Outline each blood parasite and name the species.
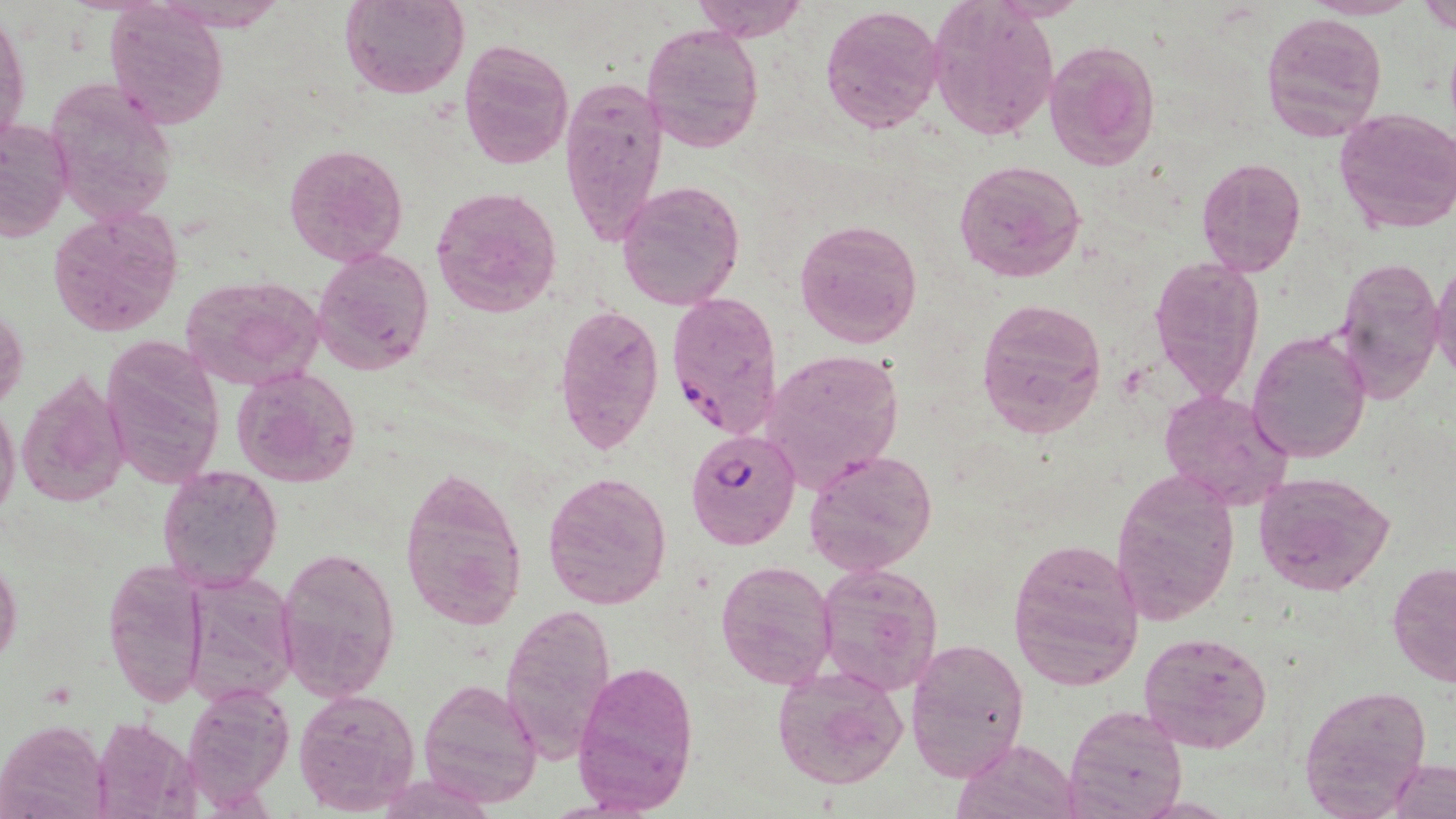

Approximate bounding boxes as [x1, y1, x2, y2] in pixels.
Plasmodium falciparum-infected red blood cells: [664, 289, 782, 441], [685, 429, 800, 548].
No Plasmodium ovale, Plasmodium malariae, Plasmodium vivax, Babesia divergens, or Trypanosoma brucei observed.

Uninfected red blood cell locations: [340, 0, 470, 100], [693, 0, 809, 43], [1419, 0, 1456, 34], [926, 1, 1058, 141], [103, 2, 229, 126], [1, 5, 29, 150], [820, 6, 946, 132], [1259, 10, 1387, 143], [642, 22, 762, 150], [458, 38, 574, 170], [1044, 39, 1162, 171], [43, 74, 179, 225], [559, 74, 668, 252], [1334, 106, 1456, 235], [0, 119, 73, 242], [284, 141, 409, 269], [954, 157, 1086, 285], [1195, 157, 1306, 277], [615, 180, 745, 310], [430, 186, 562, 317], [48, 207, 183, 338], [795, 219, 922, 348], [313, 247, 435, 373], [1149, 255, 1266, 400], [1335, 255, 1446, 403], [1431, 259, 1456, 381], [178, 273, 325, 391], [975, 297, 1107, 438], [552, 302, 665, 455], [0, 309, 28, 412], [1246, 327, 1373, 465], [98, 334, 226, 491], [758, 347, 904, 491], [233, 366, 362, 487], [16, 369, 130, 509], [1159, 388, 1294, 510], [0, 400, 20, 522], [804, 450, 937, 576], [397, 463, 529, 633], [157, 465, 284, 592], [1110, 467, 1239, 624], [542, 470, 672, 610], [1253, 471, 1395, 595], [1010, 539, 1144, 690], [276, 542, 399, 702], [0, 557, 22, 666], [715, 560, 837, 689], [1387, 561, 1456, 689], [814, 562, 944, 695], [103, 563, 208, 707], [182, 572, 298, 709], [499, 601, 619, 761], [1139, 629, 1273, 754], [904, 637, 1031, 783], [572, 659, 701, 814], [773, 664, 909, 792], [418, 678, 544, 808], [183, 685, 294, 806], [1299, 686, 1433, 813], [291, 687, 420, 813], [1064, 703, 1186, 819], [90, 717, 198, 819], [0, 719, 110, 819], [955, 738, 1080, 819], [1389, 758, 1456, 819]. Slide-level diagnosis: Plasmodium falciparum. 1000x magnification. Light microscopy. May-Grünwald-Giemsa-stained preparation. Image is 1456×819 pixels. One field of a larger specimen. Thin blood film.